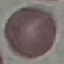
{
  "malaria_status": "uninfected",
  "preparation": "thin blood smear",
  "stain": "Giemsa",
  "image_type": "cell patch, automatically extracted from a larger field of view and resized to 64 × 64 pixels",
  "capture": "smartphone through the microscope eyepiece"
}